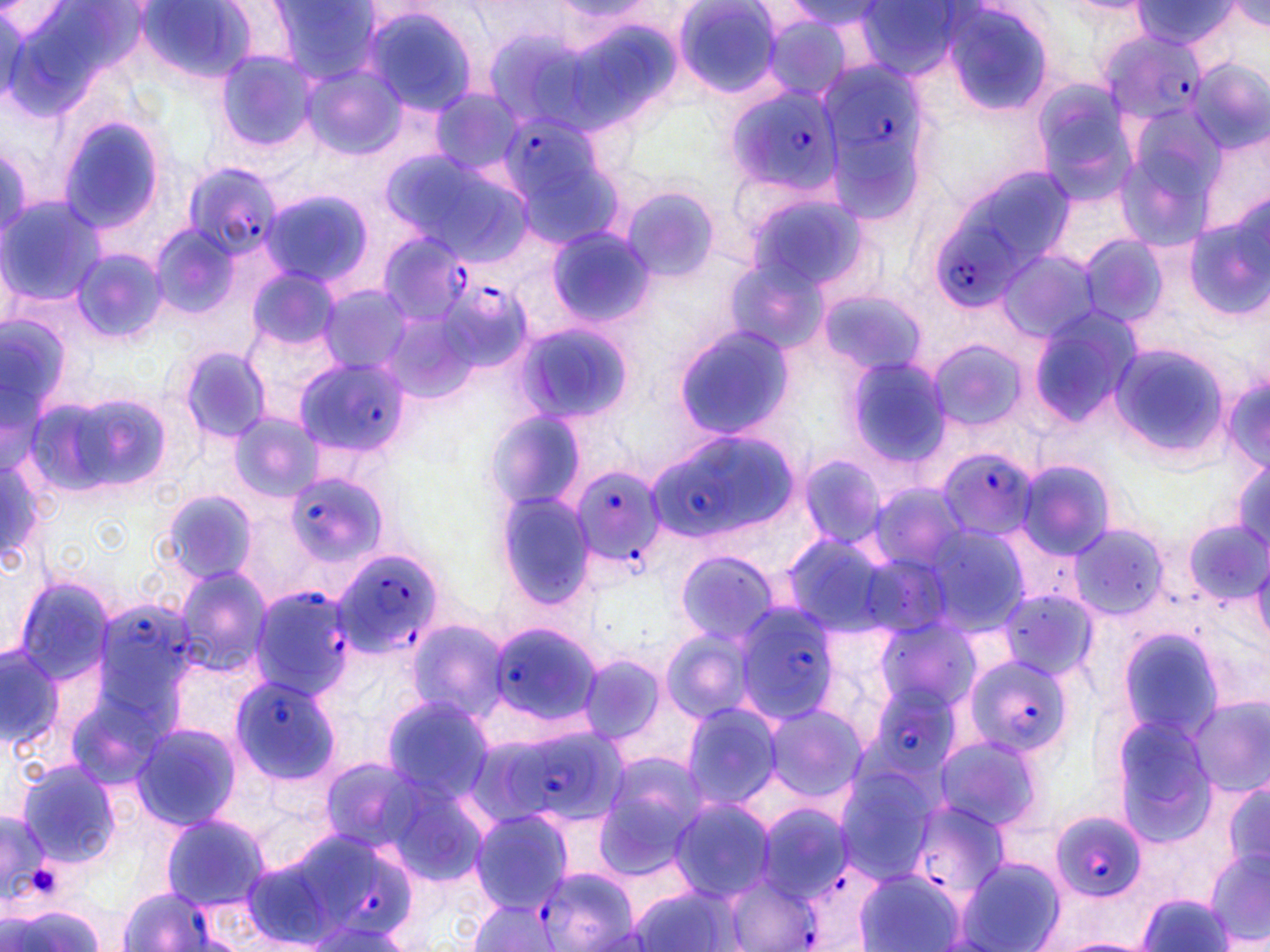
Approximate bounding boxes as [x1, y1, x2, y2] in pixels. Uninfected red blood cell locations: [272, 0, 377, 84], [674, 0, 786, 100], [936, 1, 1057, 115], [1133, 1, 1235, 50], [137, 2, 260, 85], [788, 2, 884, 26], [1223, 2, 1267, 35], [853, 3, 962, 84], [358, 5, 482, 116], [757, 13, 855, 101], [215, 50, 316, 152], [1188, 59, 1267, 153], [305, 67, 403, 159], [1033, 77, 1139, 197], [429, 89, 522, 178], [56, 113, 167, 239], [1115, 113, 1225, 247], [386, 148, 529, 266], [945, 164, 1078, 283], [623, 186, 721, 282], [260, 187, 375, 290], [738, 187, 870, 295], [1, 196, 103, 309], [1182, 209, 1270, 324], [150, 224, 240, 319], [546, 226, 654, 328], [1078, 234, 1166, 329], [997, 247, 1101, 343], [71, 248, 167, 343], [722, 256, 825, 356], [249, 266, 340, 354], [318, 284, 413, 375], [817, 289, 923, 376], [1028, 306, 1142, 427], [0, 314, 68, 421], [513, 319, 636, 426], [673, 325, 796, 441], [929, 340, 1027, 433], [1109, 343, 1226, 458], [178, 345, 272, 445], [842, 354, 952, 468], [1221, 368, 1270, 473], [53, 389, 174, 498], [486, 407, 591, 514], [230, 413, 320, 501], [799, 452, 888, 548], [1229, 455, 1270, 554], [1016, 459, 1116, 560], [160, 491, 257, 585], [497, 492, 597, 606], [1184, 517, 1268, 605], [915, 521, 1032, 636], [1066, 522, 1170, 620], [673, 549, 781, 647], [1249, 549, 1270, 646], [174, 567, 272, 673], [12, 574, 118, 684], [870, 615, 985, 719], [406, 618, 508, 724], [1114, 627, 1231, 743], [660, 628, 758, 724], [1, 645, 65, 754], [577, 654, 668, 748], [1183, 693, 1269, 798], [379, 694, 494, 804], [680, 701, 785, 809], [763, 703, 865, 804], [1112, 715, 1216, 841], [131, 721, 241, 831], [930, 731, 1047, 834], [595, 752, 709, 871], [16, 761, 124, 867], [833, 766, 938, 879], [1224, 779, 1270, 869], [667, 796, 777, 900], [468, 810, 574, 912], [160, 813, 270, 911], [1204, 849, 1270, 948], [953, 857, 1065, 952], [855, 870, 963, 952], [626, 878, 743, 952], [1137, 892, 1234, 952], [470, 897, 561, 951], [4, 904, 107, 952]. Platelet locations: [29, 864, 63, 899]. Plasmodium falciparum-infected red blood cell locations: [1099, 29, 1208, 126], [816, 57, 930, 153], [723, 85, 843, 195], [499, 113, 602, 204], [181, 165, 281, 261], [930, 221, 1020, 307], [377, 229, 480, 336], [441, 281, 531, 369], [292, 357, 407, 460], [645, 433, 799, 543], [935, 445, 1041, 549], [567, 463, 667, 574], [286, 471, 384, 572], [336, 552, 443, 654], [250, 585, 357, 699], [732, 602, 838, 723], [97, 603, 198, 686], [486, 623, 603, 727], [960, 653, 1080, 760], [229, 674, 341, 784], [876, 685, 957, 775], [505, 735, 595, 810], [905, 798, 1011, 903], [757, 803, 852, 899], [1050, 812, 1147, 903], [321, 854, 419, 939], [533, 869, 638, 949], [723, 871, 820, 952], [118, 887, 222, 952]. Slide-level diagnosis: Plasmodium falciparum. Image is 1270×952 pixels. Thin blood film. May-Grünwald-Giemsa stain. 1000x magnification. Light microscopy. One field of a larger specimen.